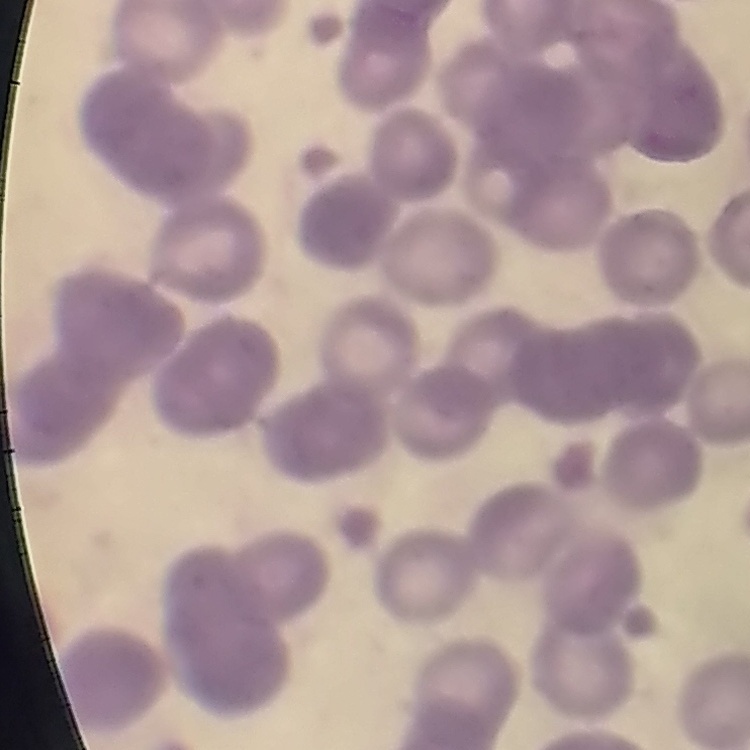
{
  "erythrocyte_morphology": "rouleaux formation",
  "preparation": "thin peripheral smear",
  "stain": "Field's or Giemsa",
  "image_type": "square crop of a larger photomicrograph"
}